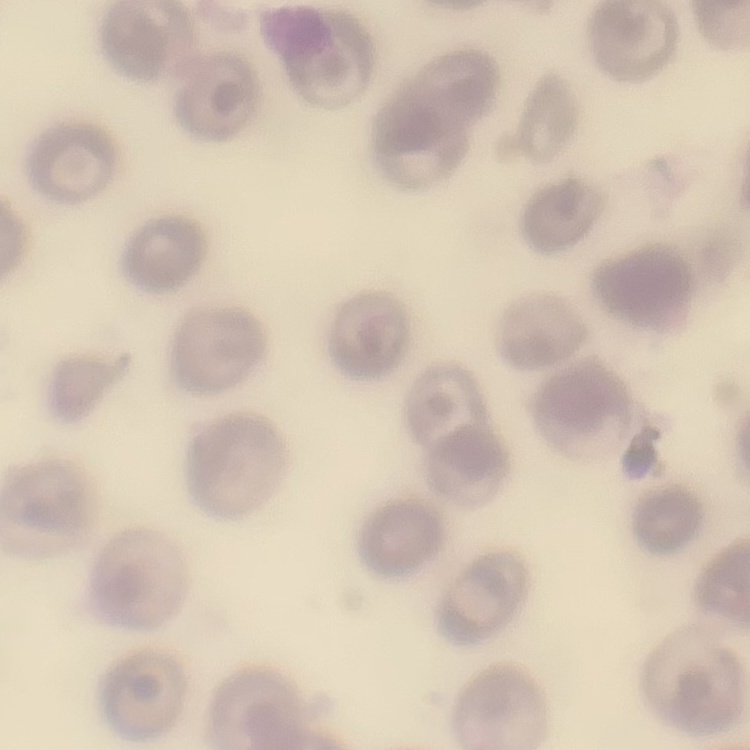

Summary:
  - Erythrocyte morphology: no rouleaux formation
  - Stain: Field's or Giemsa
  - Image type: square crop of a larger photomicrograph
  - Preparation: thin blood film